State the blood parasite species.
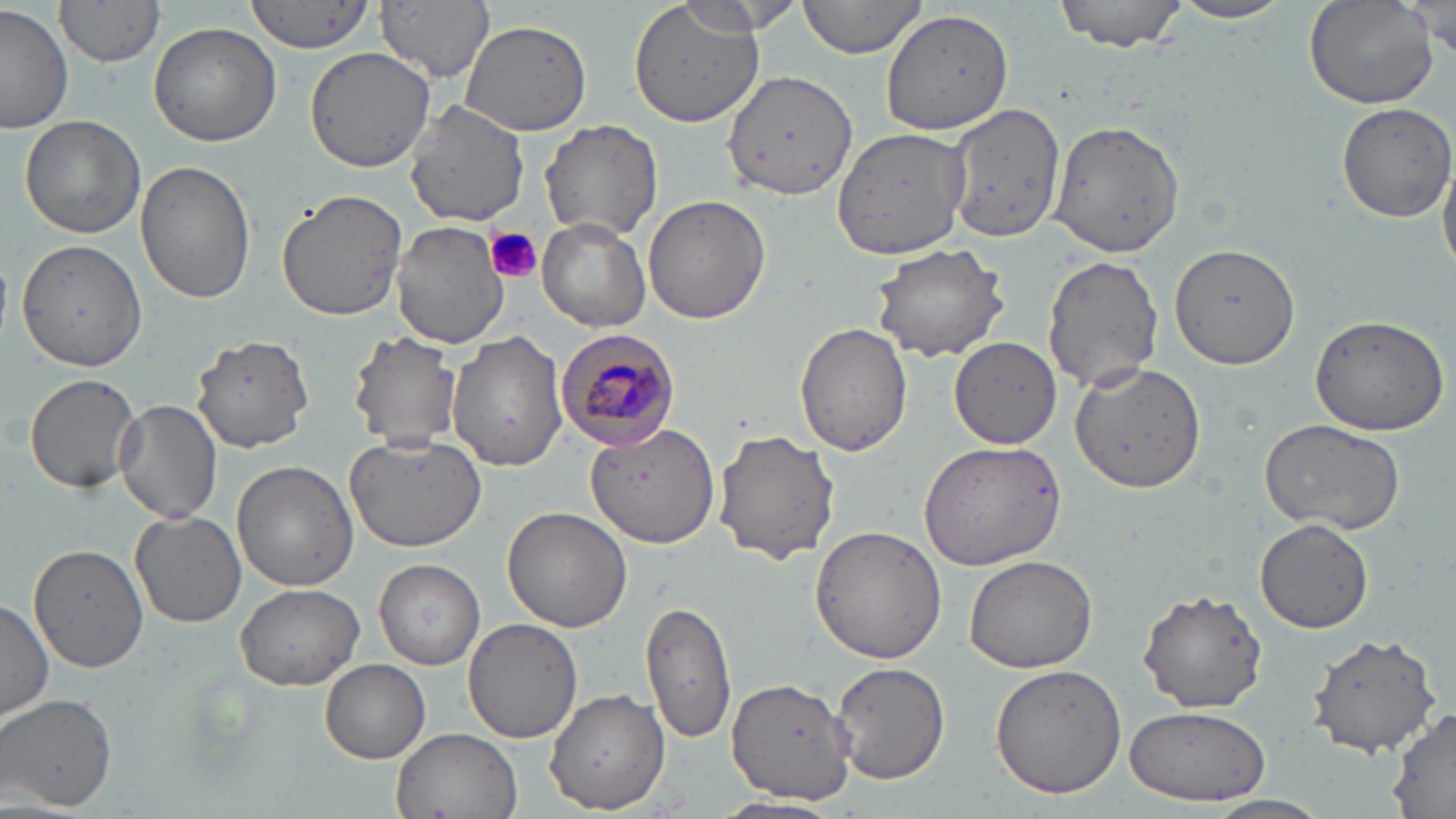

Plasmodium malariae.

{
  "uninfected_red_blood_cell_locations": "approximate bounding boxes as [x1, y1, x2, y2] in pixels: [247, 0, 371, 53], [376, 0, 495, 82], [627, 0, 767, 128], [799, 0, 930, 58], [1054, 0, 1189, 50], [1305, 0, 1438, 110], [56, 1, 165, 69], [672, 1, 803, 36], [1168, 1, 1296, 25], [1411, 2, 1455, 60], [0, 3, 75, 136], [880, 8, 1015, 137], [458, 19, 592, 135], [148, 22, 281, 147], [305, 45, 440, 175], [723, 69, 858, 202], [1335, 100, 1456, 222], [404, 102, 528, 226], [946, 104, 1066, 244], [20, 115, 148, 239], [541, 119, 665, 241], [1051, 122, 1186, 259], [828, 125, 968, 259], [1439, 144, 1456, 280], [135, 160, 253, 305], [276, 188, 408, 323], [643, 193, 768, 326], [537, 218, 651, 331], [391, 221, 507, 351], [871, 241, 1010, 363], [1168, 244, 1300, 368], [1042, 254, 1162, 393], [1308, 315, 1451, 433], [795, 321, 912, 456], [444, 329, 569, 470], [347, 332, 461, 449], [191, 333, 316, 454], [949, 338, 1061, 450], [1068, 363, 1207, 496], [23, 372, 145, 493], [114, 398, 223, 524], [1259, 419, 1408, 537], [584, 422, 721, 550], [713, 428, 842, 563], [342, 433, 486, 554], [920, 441, 1065, 571], [232, 460, 359, 592], [503, 506, 631, 632], [131, 509, 248, 628], [1256, 520, 1374, 634], [811, 525, 948, 664], [30, 543, 149, 673], [964, 556, 1099, 675], [374, 560, 484, 670], [235, 582, 363, 691], [1139, 588, 1269, 714], [640, 594, 734, 746], [0, 597, 52, 725], [462, 617, 582, 744], [1308, 631, 1442, 756], [320, 659, 430, 762], [829, 660, 952, 785], [989, 663, 1129, 798], [728, 678, 855, 804], [544, 688, 669, 810], [1, 691, 119, 812], [1123, 706, 1273, 806], [1387, 709, 1456, 816], [392, 727, 522, 819], [710, 795, 846, 819], [1203, 797, 1332, 819]",
  "field_of_view": "one of a larger specimen",
  "image_size": "1456×819 pixels",
  "stain": "May-Grünwald-Giemsa",
  "modality": "light microscopy",
  "preparation": "thin blood film",
  "platelet_locations": "approximate bounding boxes as [x1, y1, x2, y2] in pixels: [485, 228, 543, 284]",
  "magnification": "1000x",
  "plasmodium_malariae_infected_red_blood_cell_locations": "approximate bounding boxes as [x1, y1, x2, y2] in pixels: [554, 326, 682, 453]"
}